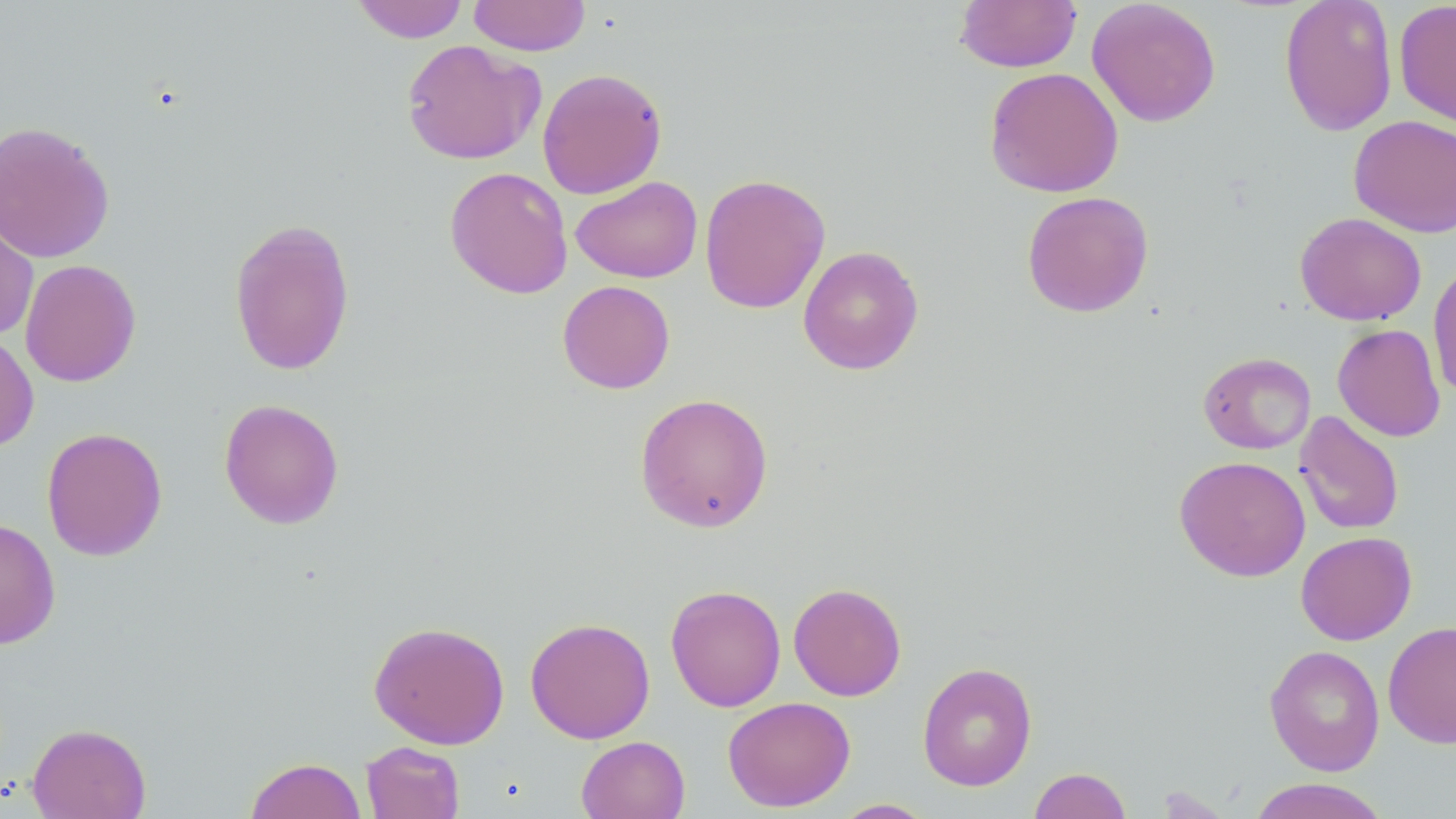

Summary:
  - Coordinate format: approximate bounding boxes as (x1, y1, x2, y2) in pixels
  - Uninfected red blood cell locations: (350, 0, 470, 43), (468, 0, 591, 56), (954, 0, 1082, 72), (1087, 0, 1221, 127), (1279, 0, 1398, 136), (1393, 1, 1456, 129), (401, 38, 543, 166), (984, 66, 1123, 198), (537, 67, 668, 199), (1349, 114, 1456, 237), (0, 120, 115, 264), (444, 166, 573, 299), (699, 173, 831, 314), (570, 176, 703, 283), (1021, 191, 1154, 317), (0, 211, 39, 341), (1295, 211, 1427, 326), (229, 217, 356, 376), (797, 245, 924, 375), (20, 258, 141, 387), (1428, 259, 1456, 399), (557, 280, 675, 394), (1332, 323, 1446, 442), (0, 330, 39, 453), (1198, 351, 1316, 454), (634, 392, 774, 533), (219, 398, 344, 529), (1294, 411, 1405, 535), (41, 427, 167, 562), (1174, 455, 1310, 582), (0, 518, 61, 650), (1295, 531, 1417, 645), (788, 582, 907, 701), (665, 584, 786, 712), (525, 617, 655, 743), (369, 620, 510, 749), (1383, 621, 1456, 748), (1264, 644, 1385, 776), (917, 661, 1037, 791), (723, 696, 856, 812), (27, 722, 151, 819), (576, 735, 690, 819), (361, 740, 465, 819), (245, 757, 367, 819), (1028, 767, 1132, 819), (1246, 778, 1392, 819), (831, 798, 936, 818)
  - Slide-level diagnosis: no evidence of blood parasites
  - Field of view: single
  - Magnification: 1000x
  - Modality: optical microscopy
  - Image size: 1456×819 pixels
  - Preparation: thin blood smear
  - Stain: May-Grünwald-Giemsa